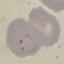

result: malaria parasites identified
preparation: thin blood film
stain: Giemsa
image_type: automatically extracted cell patch, resized to 64 × 64 pixels
capture: smartphone through the microscope eyepiece